Report the malaria status of this cell.
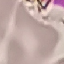

It is uninfected.

image type = automatically extracted cell patch, resized to 64 × 64 pixels
stain = Giemsa
capture = smartphone camera at the microscope eyepiece
preparation = thin blood smear